State the preparation type.
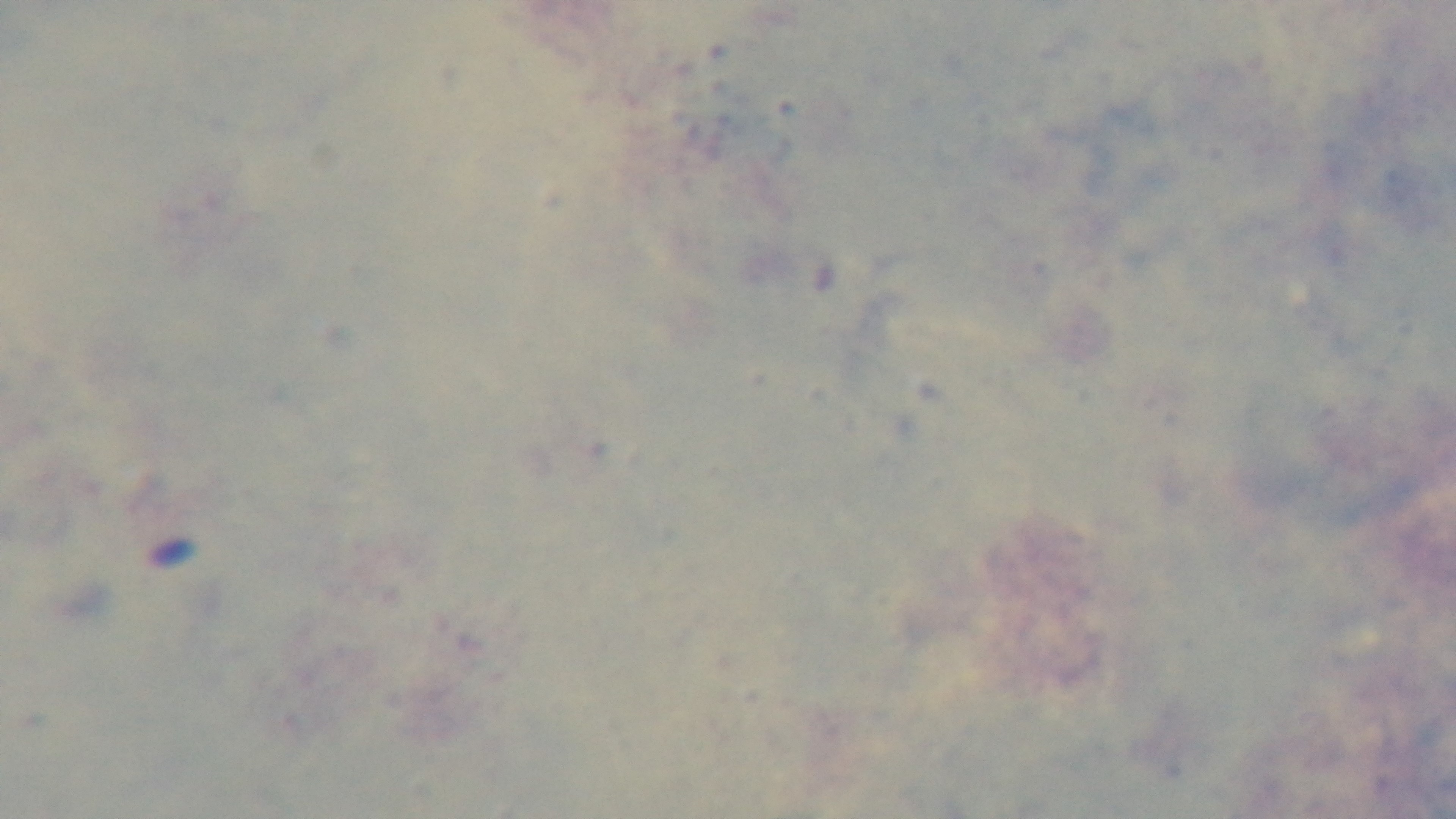

A thick smear.

One field from the slide. Mounted 4K digital camera. Giemsa stain. 100x oil-immersion objective. Malaria status: uninfected. Light microscopy.